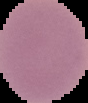
preparation = thin blood smear
image type = cell region segmented out of the field of view; surrounding area masked to black
image size = 88×103 pixels
malaria status = uninfected